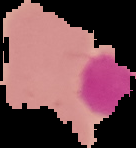

Summary:
  - Image type: segmented cell region on a black background
  - Image size: 136×148 pixels
  - Preparation: thin blood film
  - Result: no Plasmodium parasites detected